Describe the morphology of the red blood cells.
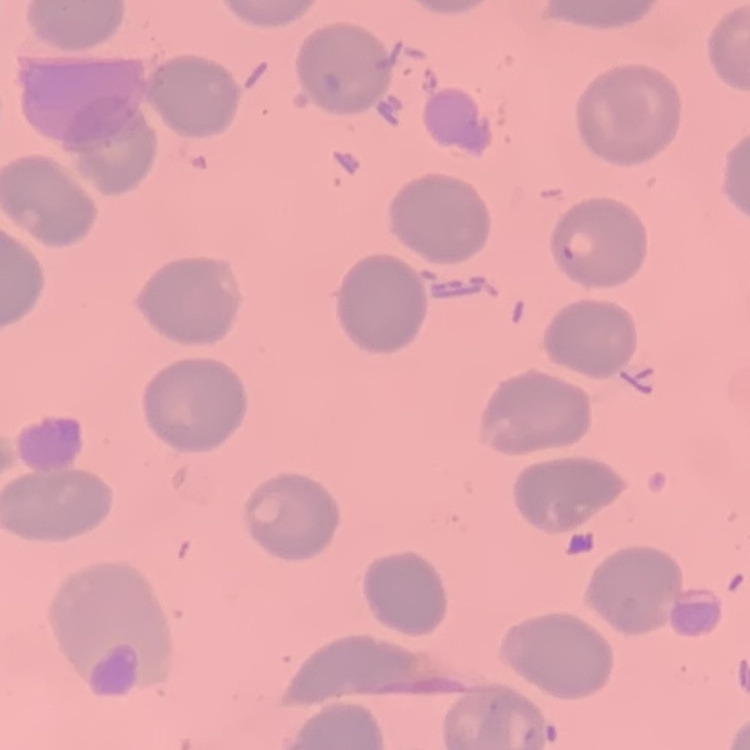
They show no rouleaux formation.

Summary:
  - Preparation: thin blood smear
  - Stain: Field's or Giemsa
  - Image type: square crop of a larger photomicrograph